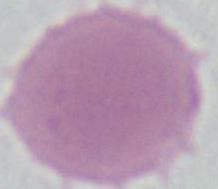

{
  "magnification": "1000x",
  "identification": "erythrocyte",
  "modality": "photomicrograph"
}